Classify this cell by malaria status.
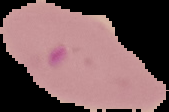
Parasitized.

Image is 169×112 pixels. Segmented cell region on a black background. From a thin blood film.